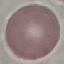
Result: negative for malaria parasites. Automatically extracted cell patch, resized to 64 × 64 pixels. Photographed with a smartphone camera at the microscope eyepiece. Thin blood smear. Giemsa stain.